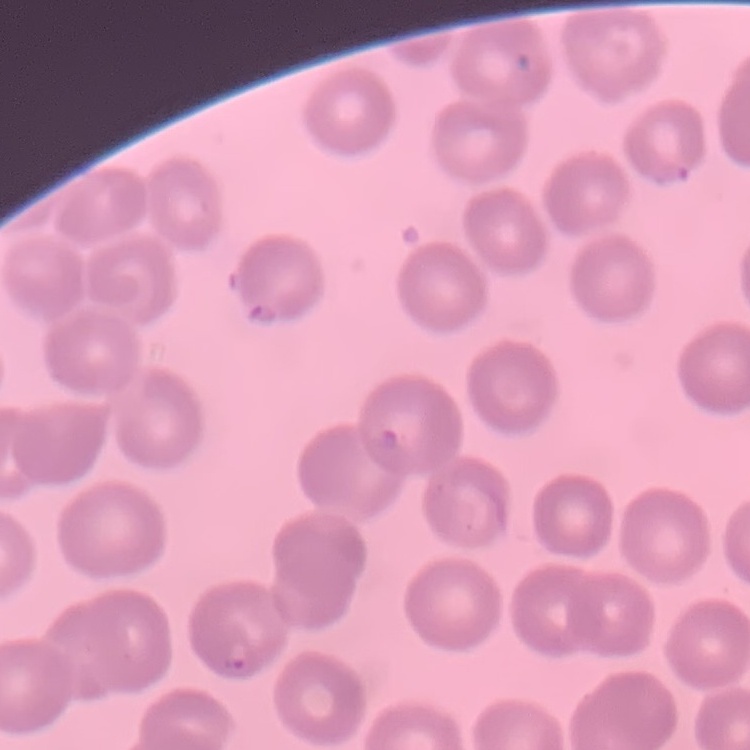

red blood cell morphology = no rouleaux formation
image type = square crop of a larger photomicrograph
preparation = thin peripheral smear
stain = Field's or Giemsa